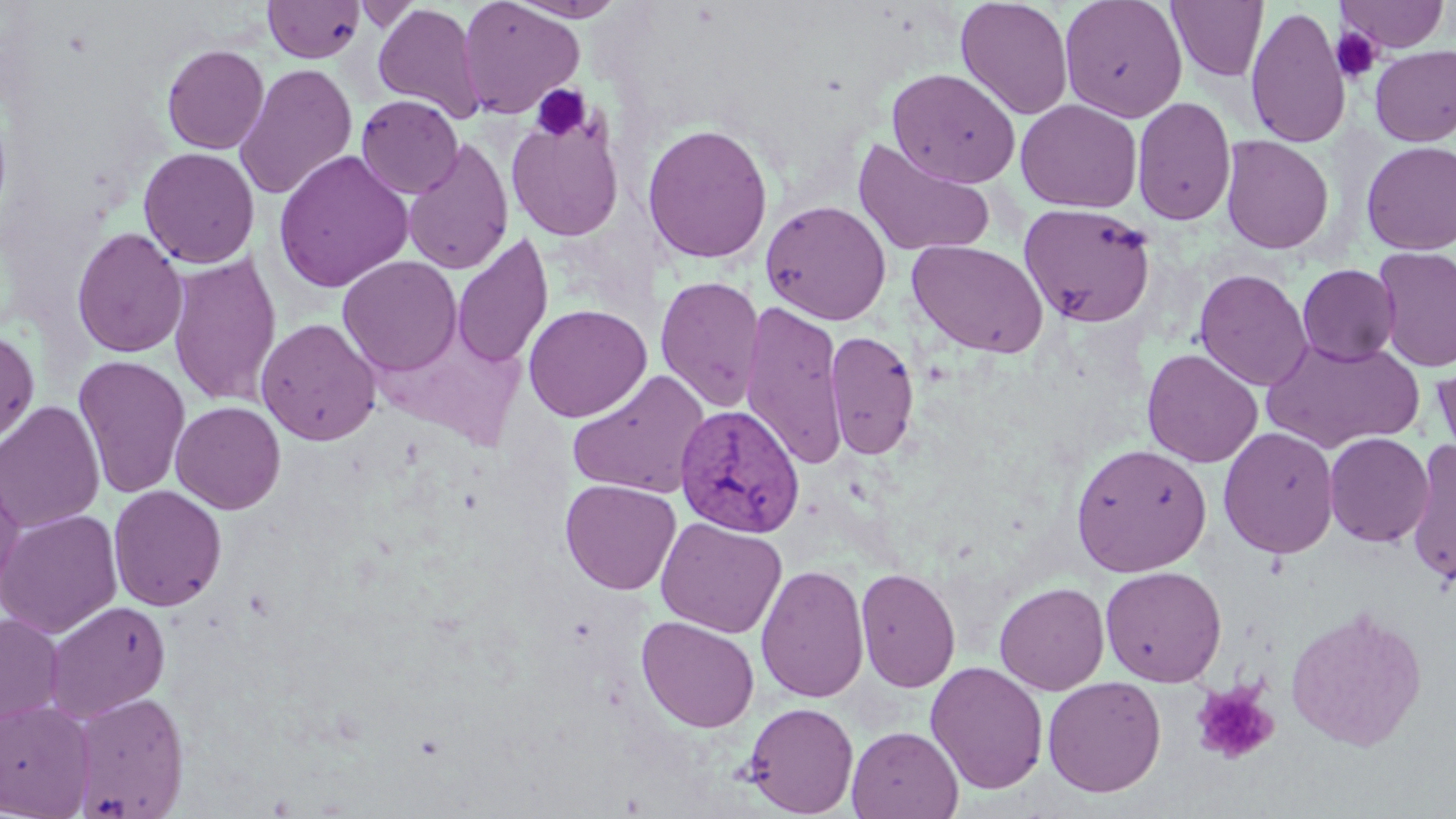

slide_level_diagnosis: Plasmodium vivax
uninfected_red_blood_cell_locations: 'approximate bounding boxes as (x1,y1)-(x2,y2) corner pairs in pixels: (508,0)-(630,21), (955,0)-(1074,119), (1059,0)-(1188,122), (1337,0)-(1451,52), (262,1)-(365,63), (457,1)-(584,119), (1168,1)-(1268,82), (352,3)-(424,32), (372,3)-(486,124), (1244,5)-(1351,148), (162,44)-(269,154), (1370,44)-(1456,146), (233,63)-(358,200), (887,67)-(1021,188), (356,95)-(463,199), (1132,96)-(1237,226), (1016,99)-(1142,213), (506,112)-(625,242), (641,123)-(774,264), (1220,135)-(1334,255), (403,137)-(515,275), (852,138)-(997,258), (1360,141)-(1456,255), (138,147)-(260,268), (272,151)-(414,293), (760,200)-(892,325), (1019,203)-(1157,328), (71,227)-(188,358), (450,233)-(554,370), (908,239)-(1049,358), (1375,246)-(1455,373), (167,251)-(282,409), (338,255)-(462,377), (1297,264)-(1400,365), (1194,268)-(1313,391), (655,275)-(766,412), (740,300)-(848,472), (522,303)-(652,423), (256,317)-(381,446), (824,329)-(919,460), (0,330)-(39,445), (1261,337)-(1424,453), (1142,348)-(1263,467), (73,355)-(191,499), (1430,359)-(1456,466), (567,369)-(712,500), (0,400)-(105,533), (171,400)-(286,513), (1218,426)-(1340,559), (1324,432)-(1433,547), (1405,439)-(1456,588), (1070,442)-(1213,577), (0,463)-(25,604), (561,479)-(681,594), (108,485)-(228,612), (0,509)-(123,639), (655,517)-(787,638), (755,563)-(870,702), (1100,565)-(1227,687), (855,566)-(961,693), (994,581)-(1110,695), (44,600)-(171,722), (1285,605)-(1428,752), (0,613)-(64,727), (636,616)-(760,733), (925,661)-(1049,795), (1042,676)-(1166,797), (70,691)-(189,818), (0,699)-(95,817), (743,701)-(859,816), (847,726)-(963,819)'
modality: light microscopy
preparation: thin blood film
stain: May-Grünwald-Giemsa
platelet_locations: 'approximate bounding boxes as (x1,y1)-(x2,y2) corner pairs in pixels: (1332,27)-(1382,83), (530,84)-(592,142), (1191,682)-(1279,765)'
field_of_view: single
magnification: 1000x
image_size: 1456×819 pixels
plasmodium_vivax_infected_red_blood_cell_locations: 'approximate bounding boxes as (x1,y1)-(x2,y2) corner pairs in pixels: (674,404)-(805,538)'